Identify the parasite.
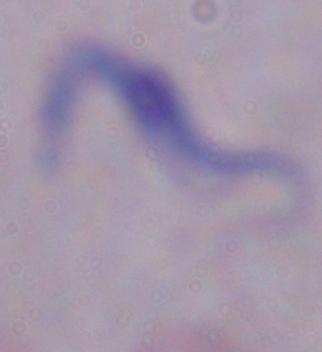
A trypanosome.

{
  "modality": "photomicrograph",
  "magnification": "1000x"
}